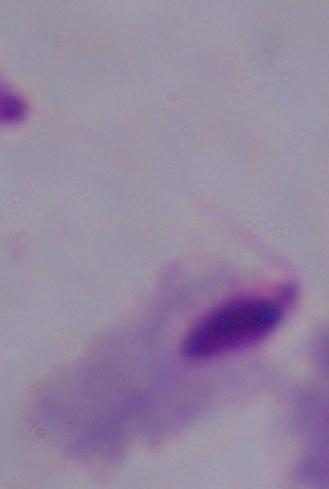 Photomicrograph. Captured at 1000x magnification. A trichomonad is seen.